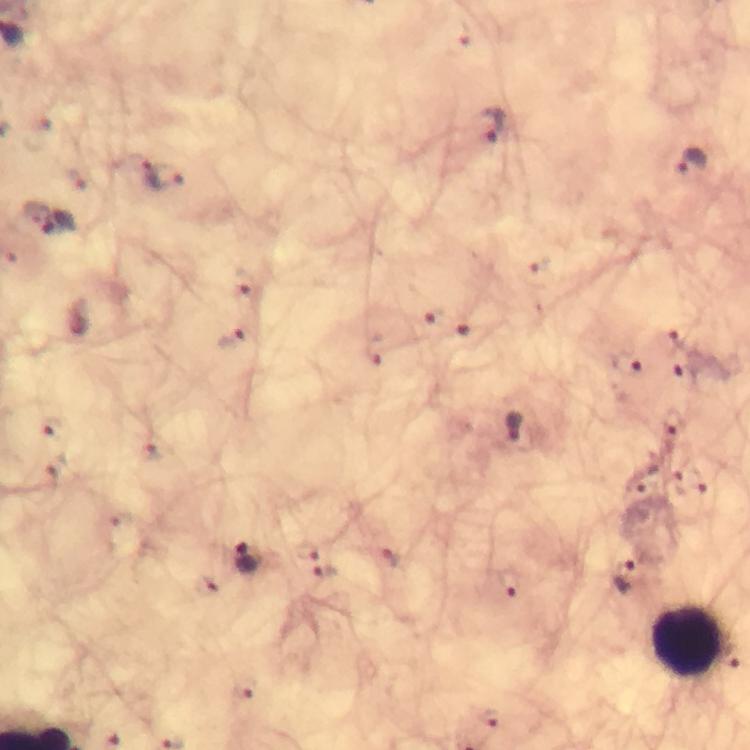
magnification = 100x
cropped from = one field of view
stain = Giemsa
leukocyte locations = approximate centers as (x, y) in pixels: (690, 642)
preparation = thick blood smear
immersion oil = applied
image size = 750×750 pixels
context = from a diagnostic examination for malaria
Plasmodium parasite locations = approximate centers as (x, y) in pixels: (493, 127), (691, 162), (162, 178), (60, 225), (242, 286), (430, 316), (473, 337), (674, 339), (230, 340), (374, 351), (628, 365), (685, 371), (672, 424), (48, 426), (518, 429), (150, 453), (57, 470), (686, 485), (305, 549), (392, 558), (248, 559), (323, 571), (626, 574), (512, 582), (245, 690)
capture = smartphone photograph through a microscope